State which cell type is depicted.
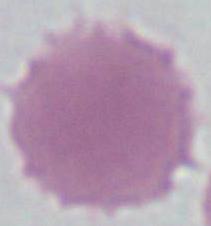

An erythrocyte.

Captured at 1000x magnification. Micrograph.